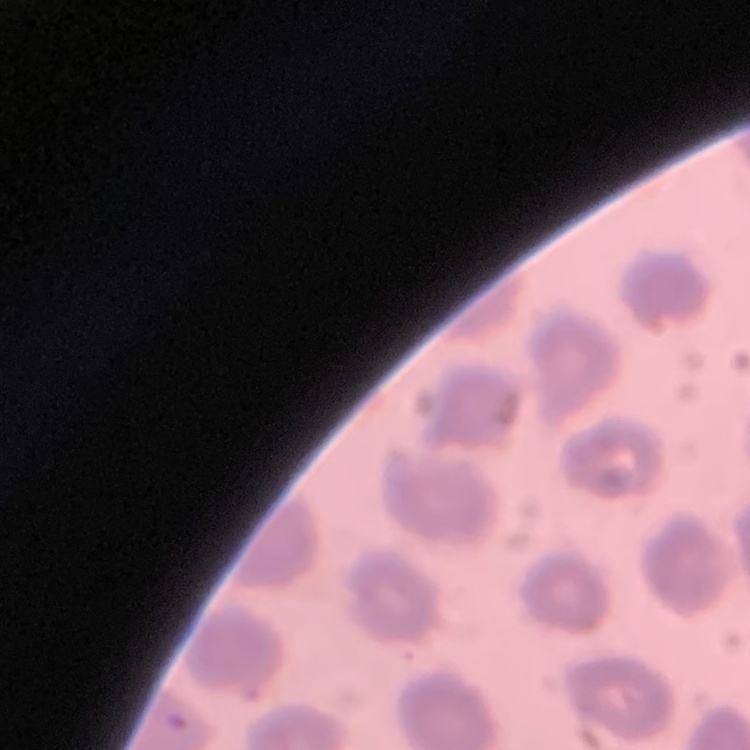
red blood cell morphology = no rouleaux formation
image type = one tile cut from a larger photomicrograph
preparation = thin peripheral smear
stain = Field's or Giemsa